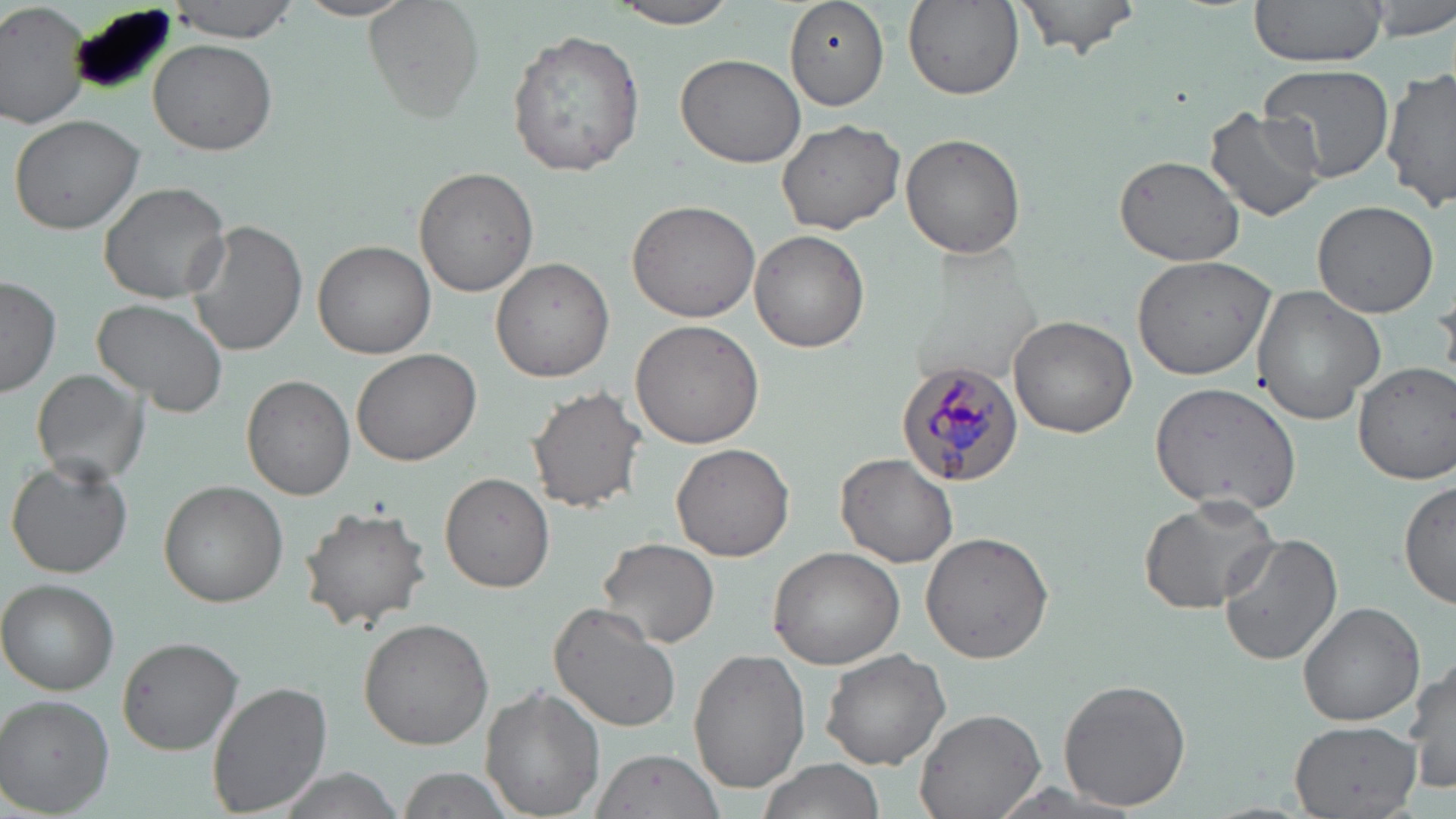

Approximate bounding boxes as (x1,y1)-(x2,y2) corner pairs in pixels. Uninfected red blood cell locations: (166,0)-(299,40), (292,0)-(418,22), (369,0)-(482,119), (1011,0)-(1141,59), (1247,0)-(1390,71), (1364,0)-(1456,40), (609,1)-(742,30), (783,1)-(888,111), (903,1)-(1024,101), (1,2)-(94,129), (66,7)-(178,100), (508,28)-(644,177), (149,37)-(279,155), (675,52)-(805,169), (1259,65)-(1395,181), (1383,71)-(1456,215), (1206,105)-(1325,222), (8,113)-(146,235), (776,119)-(905,236), (900,132)-(1028,259), (1110,135)-(1327,245), (1113,154)-(1245,266), (415,167)-(539,297), (99,180)-(231,303), (1311,199)-(1438,317), (627,200)-(760,323), (185,219)-(307,358), (750,230)-(870,352), (313,239)-(435,359), (1130,254)-(1278,381), (491,256)-(616,384), (1,276)-(60,398), (1250,286)-(1388,425), (93,298)-(226,417), (1009,317)-(1136,438), (631,318)-(767,448), (351,348)-(480,466), (1353,361)-(1456,485), (31,367)-(152,487), (242,375)-(354,499), (1149,382)-(1303,513), (526,384)-(647,513), (671,442)-(796,562), (835,453)-(959,567), (7,458)-(134,580), (440,471)-(555,592), (1401,476)-(1455,616), (159,481)-(288,607), (1136,495)-(1281,615), (297,502)-(433,631), (920,532)-(1055,663), (1215,535)-(1343,666), (597,537)-(721,649), (766,545)-(906,668), (2,580)-(119,694), (546,602)-(681,734), (1299,602)-(1424,728), (358,617)-(494,750), (116,636)-(243,755), (689,645)-(812,794), (820,648)-(950,768), (1407,657)-(1455,797), (1057,678)-(1191,811), (207,681)-(333,815), (478,683)-(605,817), (1,696)-(116,815), (915,708)-(1044,819), (1289,721)-(1423,816), (590,748)-(725,819), (756,758)-(884,819), (273,766)-(408,819), (391,767)-(517,819). Plasmodium malariae-infected red blood cell locations: (896,360)-(1023,486). Slide-level diagnosis: Plasmodium malariae. Optical microscopy. Thin blood film. Captured at 1000x magnification. Single field of view. May-Grünwald-Giemsa-stained preparation. Image is 1456×819 pixels.